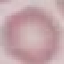

malaria status = uninfected
stain = Giemsa
preparation = thin blood smear
image type = automatically extracted cell patch, resized to 64 × 64 pixels
capture = smartphone camera at the microscope eyepiece